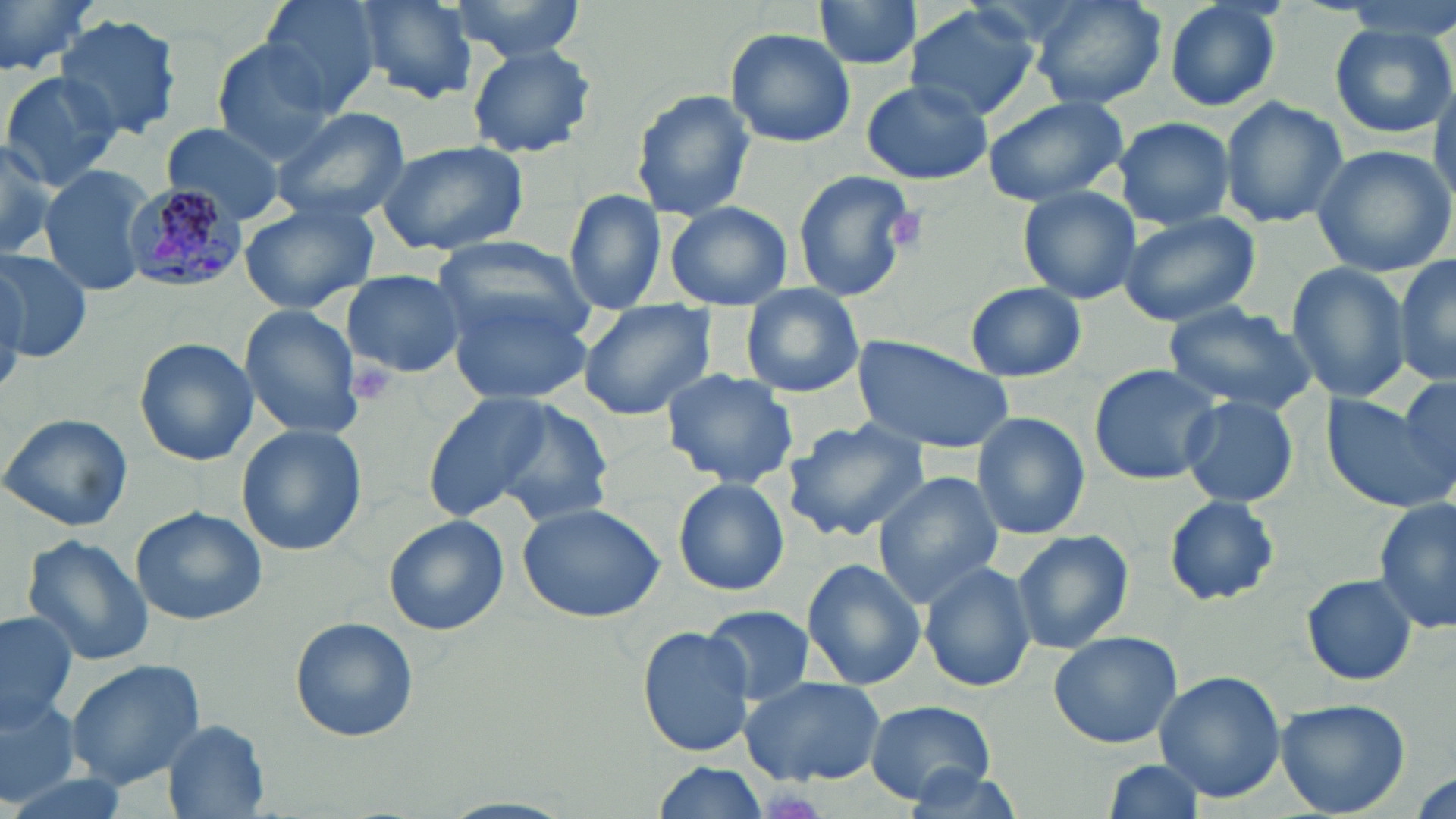

slide_level_diagnosis: Plasmodium malariae
preparation: thin blood film
uninfected_red_blood_cell_locations: 'approximate bounding boxes as (x1, y1, x2, y2) in pixels: (0, 0, 105, 79), (256, 0, 381, 112), (349, 0, 480, 104), (447, 0, 586, 58), (808, 0, 925, 72), (1030, 0, 1167, 111), (1164, 0, 1285, 113), (904, 4, 1039, 121), (55, 14, 183, 141), (1331, 21, 1453, 138), (724, 27, 856, 149), (208, 38, 347, 161), (466, 44, 597, 159), (0, 70, 123, 191), (1431, 72, 1456, 207), (861, 80, 991, 185), (629, 88, 756, 222), (980, 96, 1131, 207), (1220, 96, 1349, 228), (270, 106, 411, 224), (1112, 116, 1235, 231), (160, 122, 288, 227), (0, 136, 58, 260), (374, 139, 532, 256), (1309, 143, 1456, 279), (39, 163, 153, 298), (791, 169, 919, 303), (1017, 185, 1141, 303), (563, 189, 665, 316), (663, 200, 792, 312), (239, 201, 379, 314), (565, 202, 686, 407), (1118, 210, 1266, 328), (432, 234, 592, 341), (0, 249, 92, 362), (1393, 256, 1455, 388), (1284, 261, 1414, 406), (341, 268, 465, 379), (964, 282, 1086, 383), (739, 284, 865, 398), (444, 288, 594, 405), (577, 298, 720, 422), (1163, 301, 1318, 415), (237, 304, 365, 440), (848, 334, 1017, 456), (133, 337, 260, 467), (1088, 362, 1223, 486), (661, 369, 801, 490), (1396, 376, 1456, 489), (423, 391, 592, 525), (1321, 392, 1451, 513), (1178, 395, 1300, 510), (1, 412, 134, 532), (972, 412, 1091, 539), (783, 418, 931, 542), (235, 425, 367, 556), (872, 472, 1004, 605), (673, 477, 790, 597), (1164, 495, 1280, 605), (1373, 498, 1455, 634), (516, 502, 664, 623), (130, 505, 266, 625), (383, 515, 510, 637), (1010, 530, 1134, 653), (21, 537, 153, 668), (802, 557, 926, 688), (919, 560, 1036, 692), (1300, 573, 1419, 685), (700, 606, 816, 706), (0, 610, 79, 730), (290, 615, 419, 742), (639, 626, 757, 758), (1048, 628, 1187, 749), (66, 658, 209, 790), (1153, 670, 1286, 802), (736, 674, 885, 788), (0, 693, 83, 806), (1275, 698, 1412, 818), (864, 700, 999, 804), (162, 720, 271, 816), (1101, 760, 1206, 816), (650, 762, 771, 819), (899, 762, 1024, 818), (1407, 767, 1454, 819)'
magnification: 1000x
platelet_locations: 'approximate bounding boxes as (x1, y1, x2, y2) in pixels: (891, 207, 924, 246), (349, 362, 398, 406), (760, 791, 825, 819)'
stain: May-Grünwald-Giemsa
plasmodium_malariae_infected_red_blood_cell_locations: 'approximate bounding boxes as (x1, y1, x2, y2) in pixels: (119, 185, 247, 291)'
field_of_view: one of a larger specimen
image_size: 1456×819 pixels
modality: light microscopy